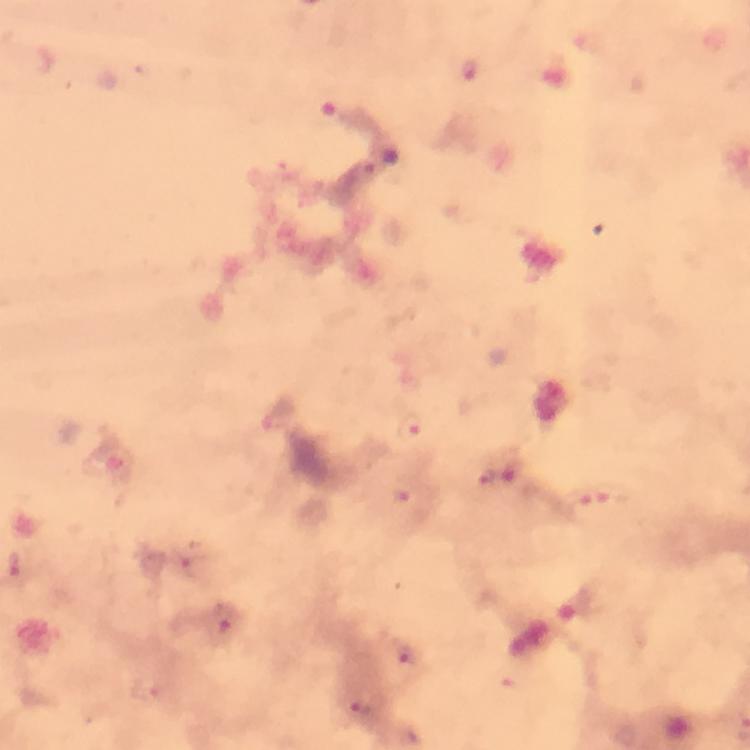
{
  "magnification": "100x",
  "stain": "Giemsa",
  "preparation": "thick blood film",
  "immersion_oil": "used",
  "cropped_from": "a single field of view",
  "context": "from a diagnostic examination for malaria",
  "image_size": "750×750 pixels",
  "plasmodium_parasite_locations": "approximate centers as (x, y) in pixels: (471, 71), (412, 428), (511, 473), (485, 476), (403, 492), (614, 498), (580, 508), (225, 627), (405, 658), (362, 706)",
  "capture": "smartphone camera through the microscope"
}